Identify the parasite.
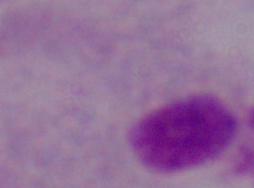
This is a trichomonad.

magnification = 1000x
modality = photomicrograph